Assess the morphology of the erythrocytes.
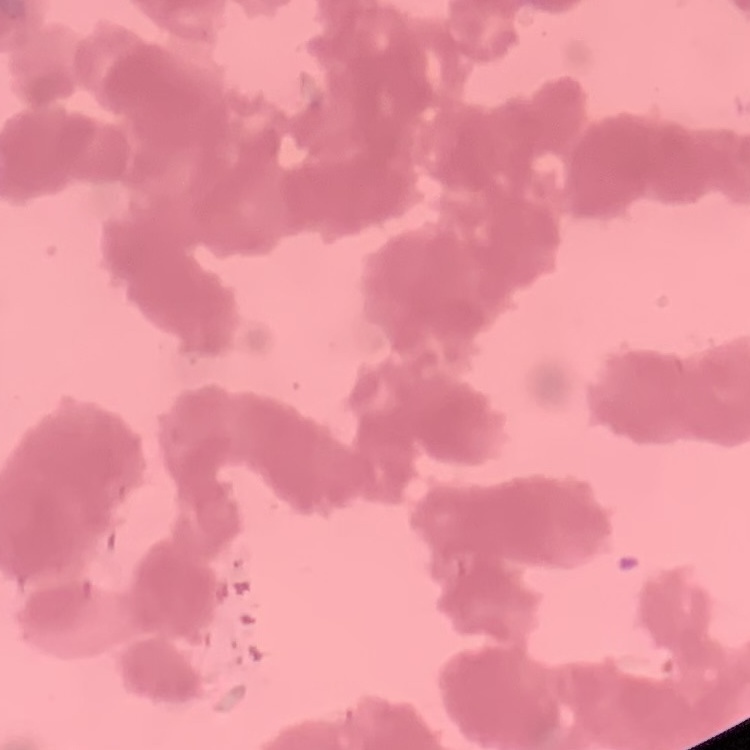
Rouleaux formation.

preparation = thin blood smear
stain = Field's or Giemsa
image type = one tile cut from a larger photomicrograph